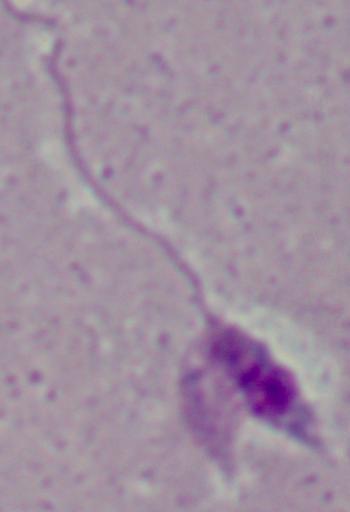

identification = Leishmania
magnification = 1000x
modality = micrograph